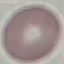
Malaria status: uninfected. Automatically extracted cell patch, resized to 64 × 64 pixels. Thin smear of blood. Acquired by smartphone through the microscope eyepiece. Giemsa-stained preparation.